State the preparation type.
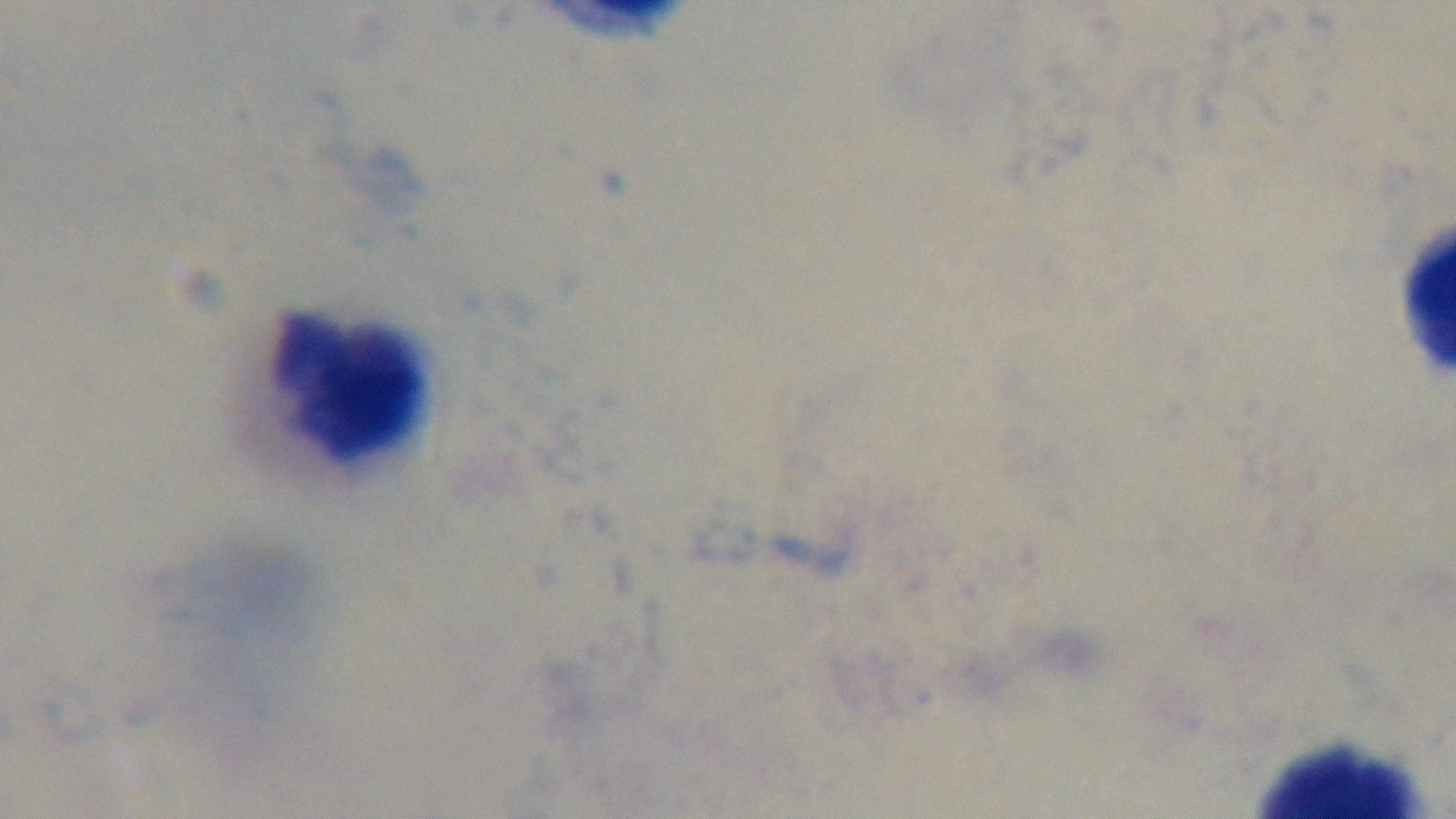
A thick smear.

Summary:
  - Modality: light microscopy
  - Objective: 100x oil immersion
  - Field of view: one from the slide
  - Malaria status: uninfected
  - Capture: mounted 4K digital camera
  - Stain: Giemsa